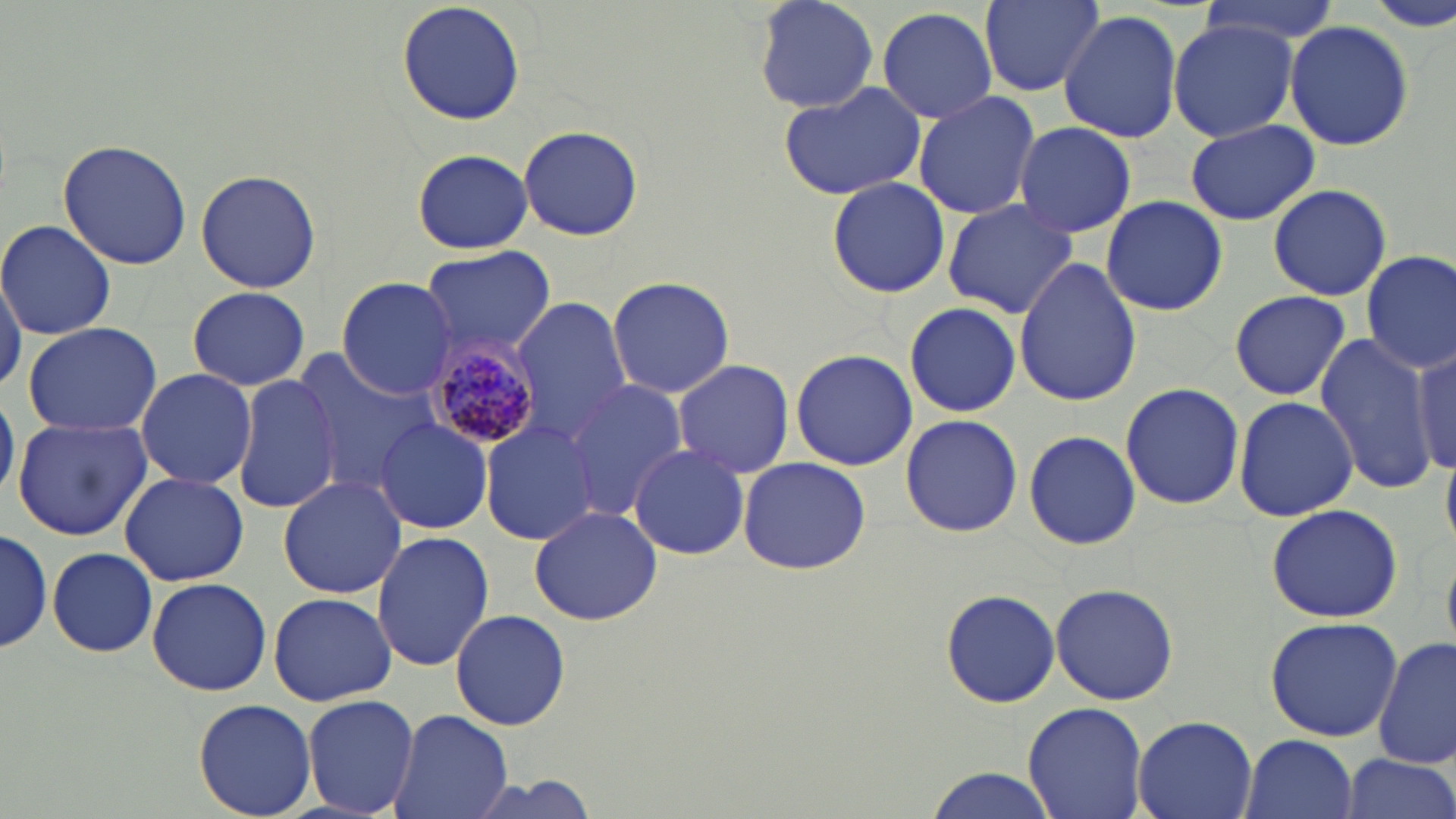
Approximate bounding boxes as (x1,y1)-(x2,y2) corner pairs in pixels. Plasmodium malariae-infected red blood cell locations: (425,332)-(544,451). Uninfected red blood cell locations: (398,0)-(524,128), (749,0)-(882,115), (980,0)-(1102,97), (1188,0)-(1343,46), (1361,0)-(1456,33), (875,5)-(997,124), (1056,10)-(1182,142), (1165,20)-(1298,142), (1284,20)-(1415,150), (775,81)-(926,201), (912,90)-(1042,219), (1185,119)-(1318,226), (1013,120)-(1136,240), (518,124)-(643,241), (57,138)-(192,269), (411,148)-(534,256), (194,168)-(322,293), (825,175)-(952,298), (1266,182)-(1392,301), (1100,195)-(1228,316), (941,199)-(1078,319), (1,218)-(117,340), (420,247)-(555,354), (1360,250)-(1456,374), (1012,258)-(1142,406), (0,264)-(23,396), (607,276)-(734,397), (336,277)-(458,400), (187,286)-(309,390), (1228,289)-(1356,400), (511,298)-(633,440), (903,301)-(1022,418), (23,322)-(162,437), (1315,335)-(1435,496), (1411,343)-(1455,478), (790,350)-(916,470), (293,351)-(441,493), (673,359)-(796,478), (135,369)-(258,492), (231,375)-(340,514), (565,379)-(691,515), (1120,383)-(1244,509), (0,389)-(19,507), (1233,395)-(1359,521), (11,413)-(153,540), (899,414)-(1024,537), (374,417)-(493,534), (481,419)-(600,549), (1023,429)-(1141,551), (629,443)-(750,561), (735,458)-(873,576), (119,472)-(250,586), (278,474)-(406,600), (1265,503)-(1405,622), (528,505)-(662,626), (0,526)-(53,654), (371,531)-(492,669), (48,547)-(157,658), (146,576)-(272,695), (1049,581)-(1180,708), (939,587)-(1060,709), (268,592)-(397,706), (449,608)-(571,730), (1265,614)-(1402,741), (1374,636)-(1456,767), (302,693)-(421,817), (194,698)-(317,818), (1023,701)-(1148,819), (389,708)-(512,819), (1132,715)-(1257,819), (1240,734)-(1357,819), (1341,757)-(1454,819), (923,768)-(1059,819). Slide-level diagnosis: Plasmodium malariae. One field of a larger specimen. Thin blood film. Light microscopy. May-Grünwald-Giemsa stain. 1000x magnification. Image is 1456×819 pixels.